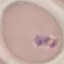

malaria status = parasitized
preparation = thin blood film
stain = Giemsa
image type = automatically extracted cell patch, resized to 64 × 64 pixels
capture = smartphone camera at the microscope eyepiece